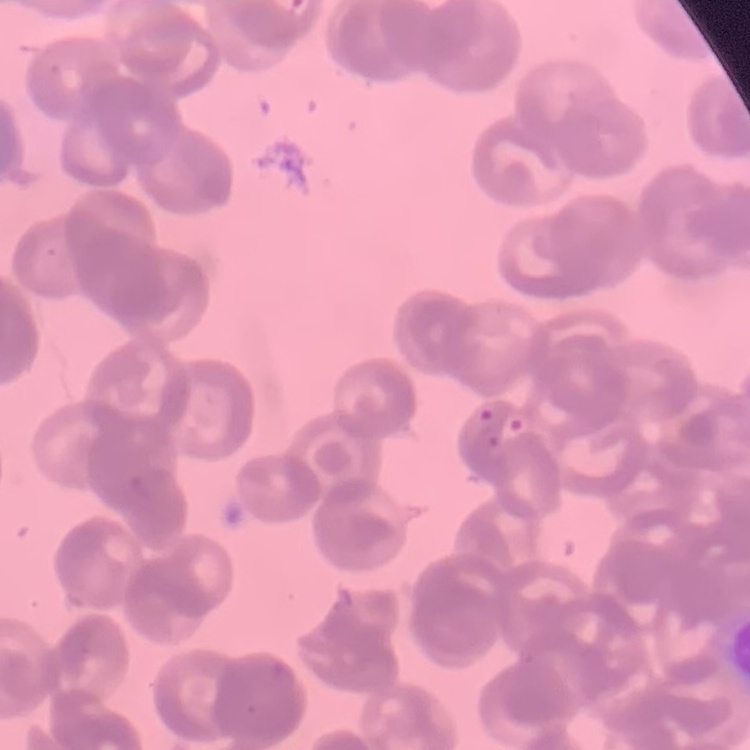
The red blood cells show rouleaux formation. Stained with either Field's or Giemsa. Square crop of a larger photomicrograph. Thin blood film.